Classify this cell by malaria status.
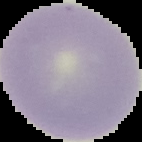

It is uninfected.

Summary:
  - Image type: cell region segmented out of the field of view; surrounding area masked to black
  - Preparation: thin blood film
  - Image size: 142×142 pixels